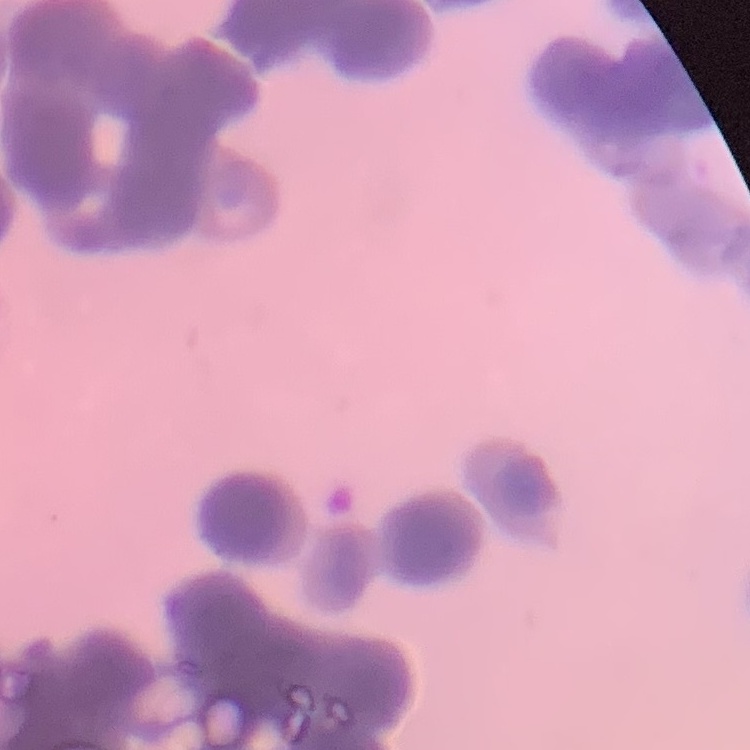

The erythrocytes exhibit rouleaux formation. One tile cut from a larger photomicrograph. Thin peripheral smear. Field's or Giemsa stain.